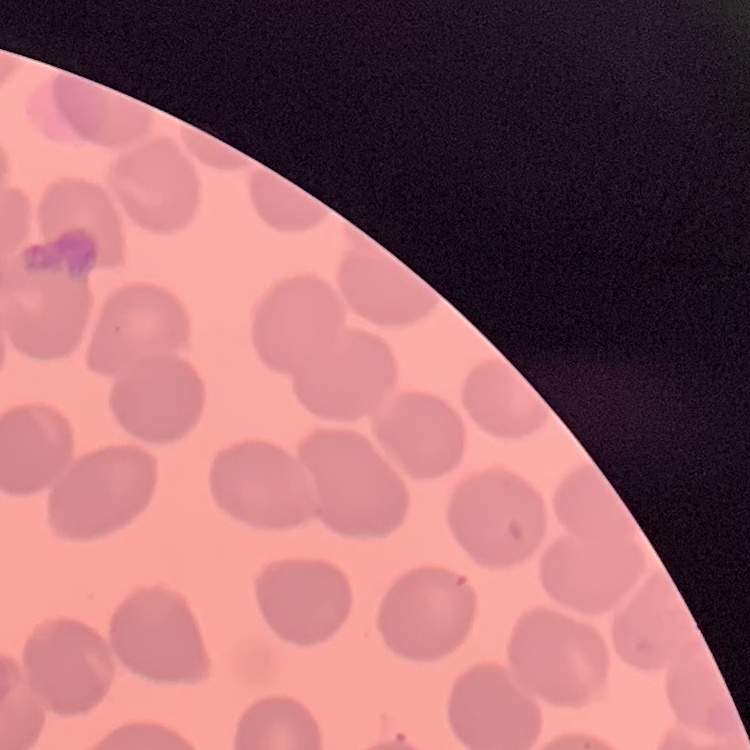

The erythrocytes show no rouleaux formation. Square crop of a larger photomicrograph. Stained with either Field's or Giemsa. Thin peripheral smear.